Assess this cell for malaria.
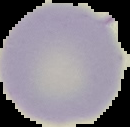

Uninfected.

Cell region segmented out of the field of view; the surrounding area is masked to black. Image is 130×127 pixels. From a thin blood film.